Classify this cell by malaria status.
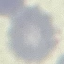
It is uninfected.

image type = automatically extracted cell patch, resized to 64 × 64 pixels
capture = smartphone camera at the microscope eyepiece
preparation = thin blood film
stain = Giemsa